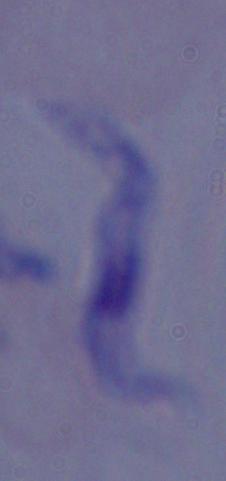
modality = photomicrograph
magnification = 1000x
identification = trypanosome